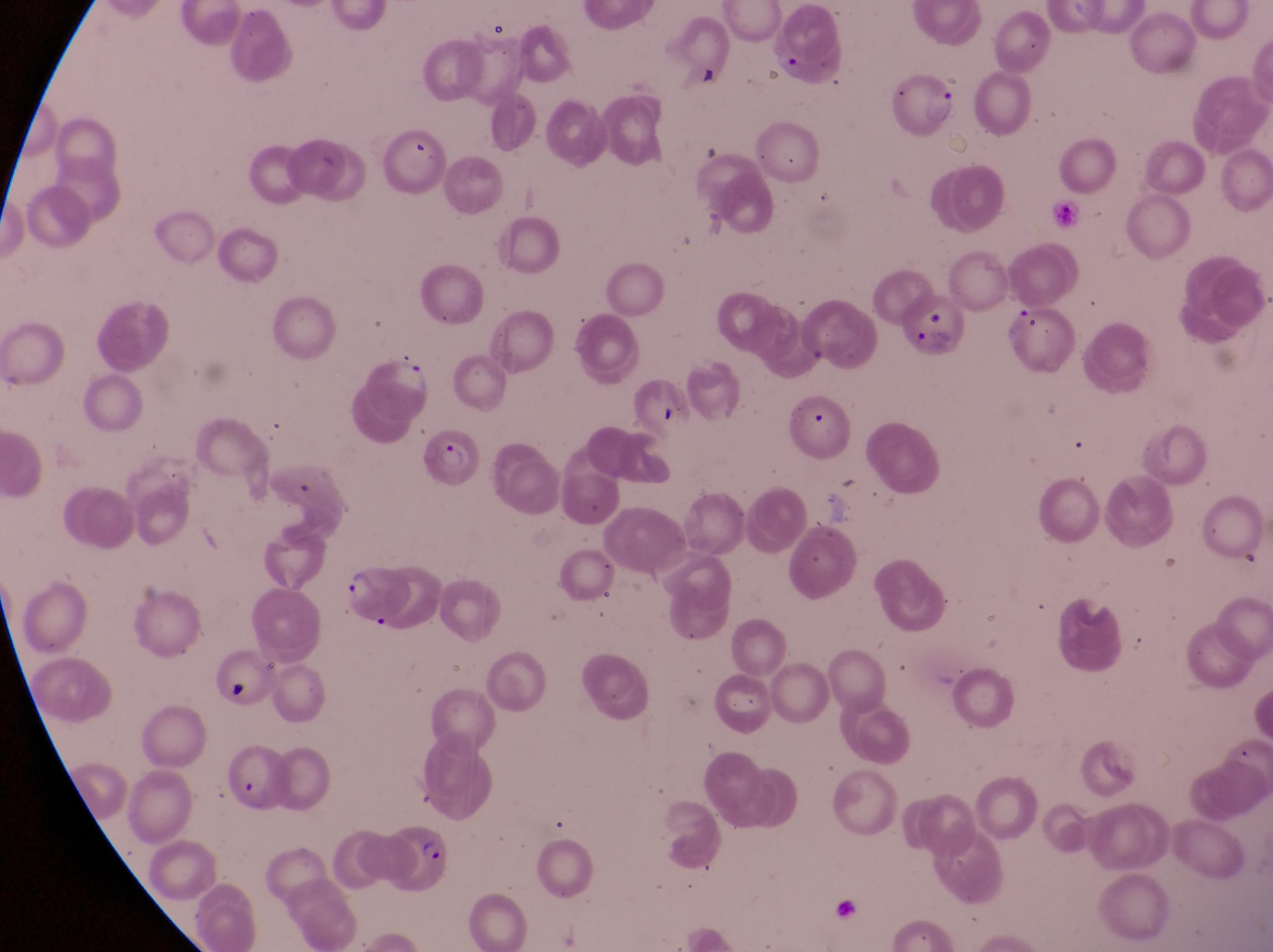

image size = 1273×952 pixels
field of view = single
capture = smartphone photograph through the eyepiece of an Olympus CX-23 microscope
parasitised red blood cell locations = approximate bounding boxes as (left, top, right, bottom) in pixels: (894, 72, 956, 139), (908, 290, 966, 358), (364, 352, 429, 422), (801, 402, 840, 441), (422, 422, 480, 494), (337, 562, 414, 630), (207, 737, 285, 812), (382, 826, 452, 900)
magnification = 1000x
preparation = thin blood smear
artifact (platelet-like body, stain precipitate, or debris) locations = approximate bounding boxes as (left, top, right, bottom) in pixels: (621, 379, 691, 439), (215, 669, 254, 709)
country = Uganda